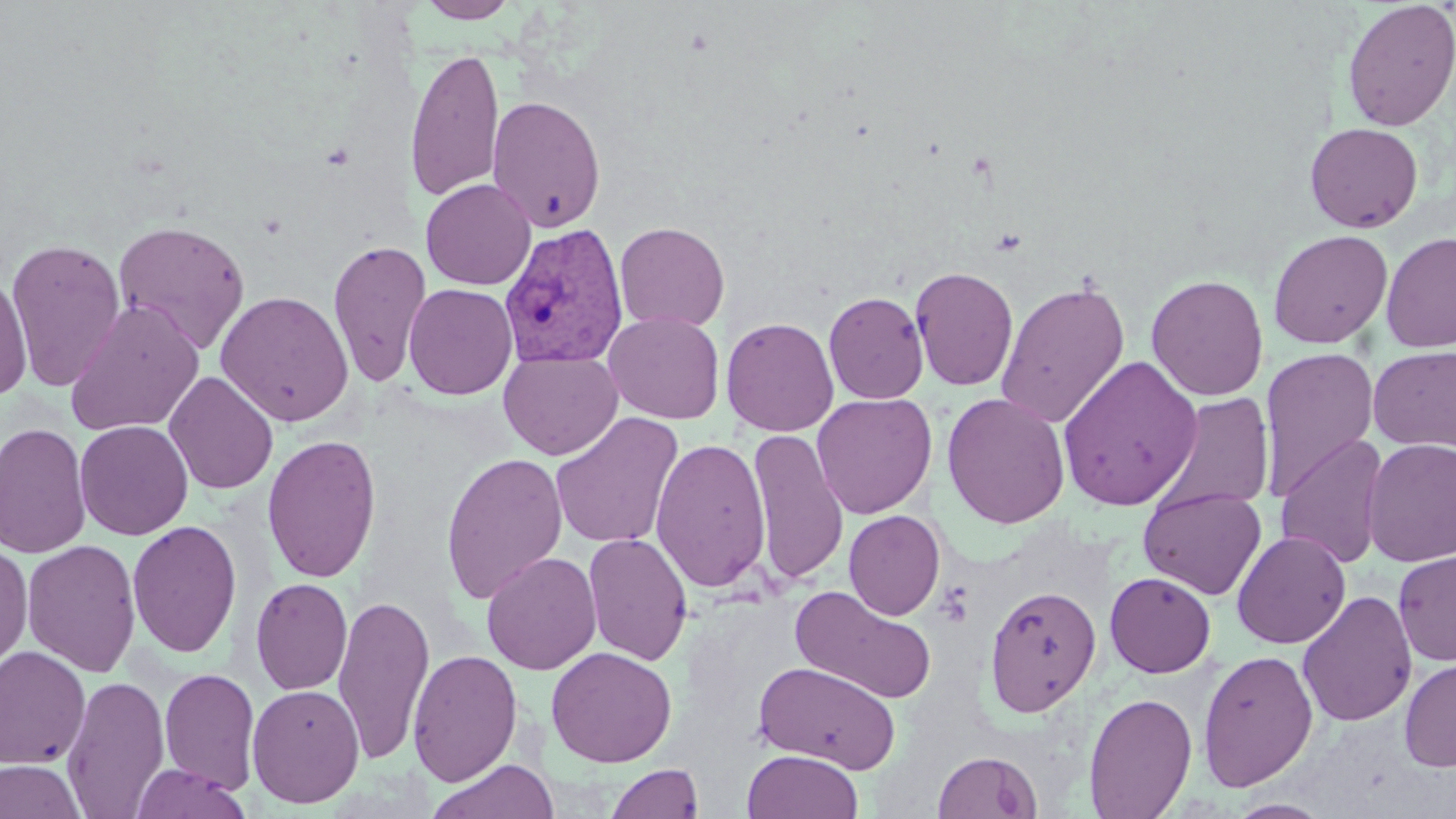
Approximate bounding boxes as (x1,y1)-(x2,y2) corner pairs in pixels. Uninfected red blood cell locations: (417,0)-(520,23), (1341,0)-(1456,132), (405,46)-(505,203), (486,94)-(607,232), (1304,122)-(1424,233), (420,178)-(537,290), (111,219)-(251,354), (614,221)-(730,333), (1268,229)-(1393,349), (1380,231)-(1456,353), (5,238)-(127,392), (328,238)-(431,387), (909,265)-(1019,392), (0,271)-(34,402), (1146,274)-(1269,401), (995,279)-(1131,429), (403,282)-(518,400), (215,290)-(355,426), (823,291)-(929,404), (65,300)-(204,437), (603,311)-(725,424), (721,316)-(840,437), (1260,345)-(1380,502), (1368,345)-(1456,452), (498,350)-(623,460), (1056,355)-(1203,511), (164,371)-(278,495), (940,391)-(1071,529), (811,392)-(936,519), (1157,393)-(1274,516), (550,412)-(684,548), (74,420)-(194,540), (0,422)-(91,558), (747,428)-(849,586), (1276,432)-(1390,570), (262,433)-(382,582), (650,437)-(771,593), (1362,437)-(1456,567), (440,451)-(569,605), (1138,486)-(1267,600), (843,510)-(945,621), (127,519)-(243,658), (1232,530)-(1351,649), (583,531)-(693,666), (22,538)-(142,678), (0,542)-(33,671), (1393,550)-(1456,666), (481,551)-(602,674), (1105,572)-(1216,678), (250,577)-(352,695), (984,585)-(1102,716), (788,586)-(939,704), (1297,590)-(1417,727), (332,595)-(436,765), (0,646)-(91,769), (546,646)-(677,767), (407,648)-(523,786), (1198,649)-(1319,792), (1398,656)-(1456,773), (752,661)-(903,773), (159,667)-(261,794), (61,673)-(170,816), (247,683)-(364,808), (1084,692)-(1197,819), (742,749)-(864,819), (932,749)-(1043,819), (1,759)-(86,818), (426,759)-(561,819), (129,763)-(252,819), (605,763)-(705,818), (1226,798)-(1335,818). Plasmodium vivax-infected red blood cell locations: (498,221)-(629,369). Slide-level diagnosis: Plasmodium vivax. Image is 1456×819 pixels. May-Grünwald-Giemsa-stained preparation. Thin blood smear. One field of a larger specimen. Captured at 1000x magnification. Optical microscopy.